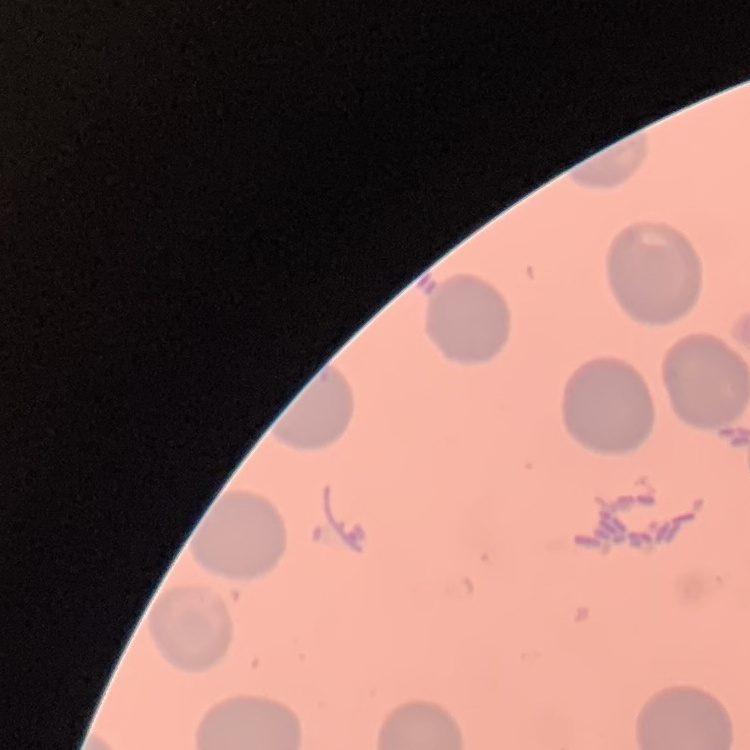
Summary:
  - Erythrocyte morphology: no rouleaux formation
  - Image type: one tile cut from a larger photomicrograph
  - Preparation: thin blood film
  - Stain: Field's or Giemsa